Identify the blood parasite species.
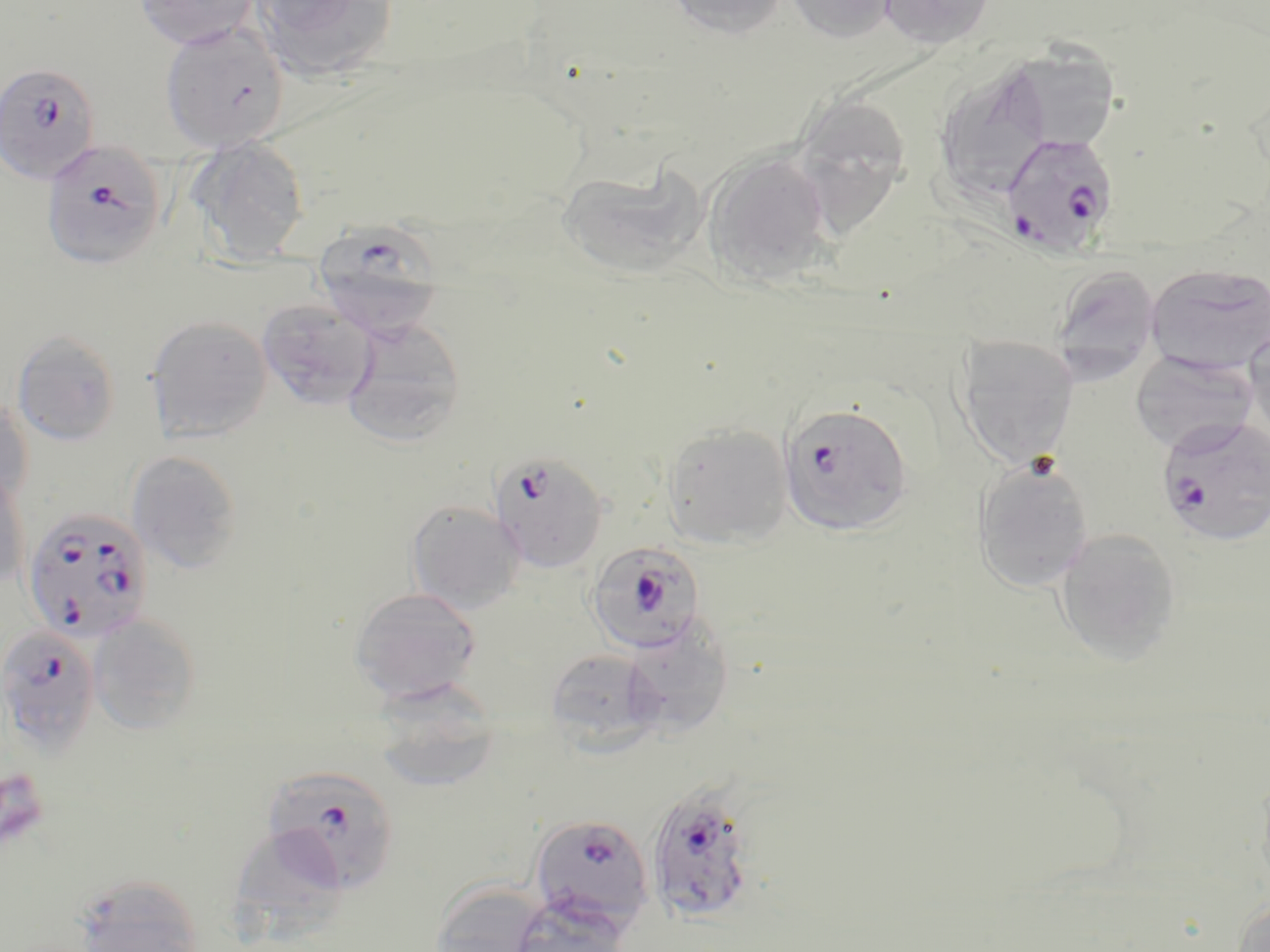

Plasmodium falciparum.

Approximate bounding boxes as (x1,y1)-(x2,y2) corner pairs in pixels. Platelet locations: (0,768)-(50,854). Uninfected red blood cell locations: (135,0)-(260,50), (252,0)-(398,81), (664,0)-(790,39), (785,0)-(897,44), (879,0)-(995,49), (159,22)-(289,153), (1003,47)-(1121,153), (933,59)-(1056,205), (792,92)-(912,233), (186,136)-(310,265), (701,151)-(836,286), (558,162)-(708,281), (1145,263)-(1270,374), (1049,264)-(1162,381), (257,299)-(377,410), (146,315)-(272,442), (343,318)-(467,445), (1244,322)-(1270,443), (12,330)-(121,446), (955,335)-(1078,469), (1129,351)-(1257,452), (0,397)-(34,509), (661,422)-(792,550), (126,450)-(243,574), (973,456)-(1095,593), (0,468)-(30,591), (406,500)-(525,614), (1054,527)-(1182,665), (349,587)-(483,706), (88,614)-(203,734), (621,615)-(734,739), (545,648)-(662,751), (371,679)-(503,793), (1255,767)-(1270,897), (229,822)-(348,938), (72,874)-(206,952), (428,879)-(555,952), (505,897)-(632,952), (1232,897)-(1270,952). Plasmodium falciparum-infected red blood cell locations: (0,60)-(102,186), (1001,133)-(1119,257), (40,139)-(168,270), (313,219)-(445,340), (778,402)-(914,537), (1156,415)-(1270,547), (489,450)-(609,574), (22,507)-(154,643), (586,541)-(704,655), (0,624)-(102,755), (263,763)-(402,894), (645,783)-(759,925), (529,815)-(655,931). Captured at 1000x magnification. Thin blood smear. Single field of view. Optical microscopy. Image is 1270×952 pixels. May-Grünwald-Giemsa-stained preparation.